Look for Plasmodium parasites.
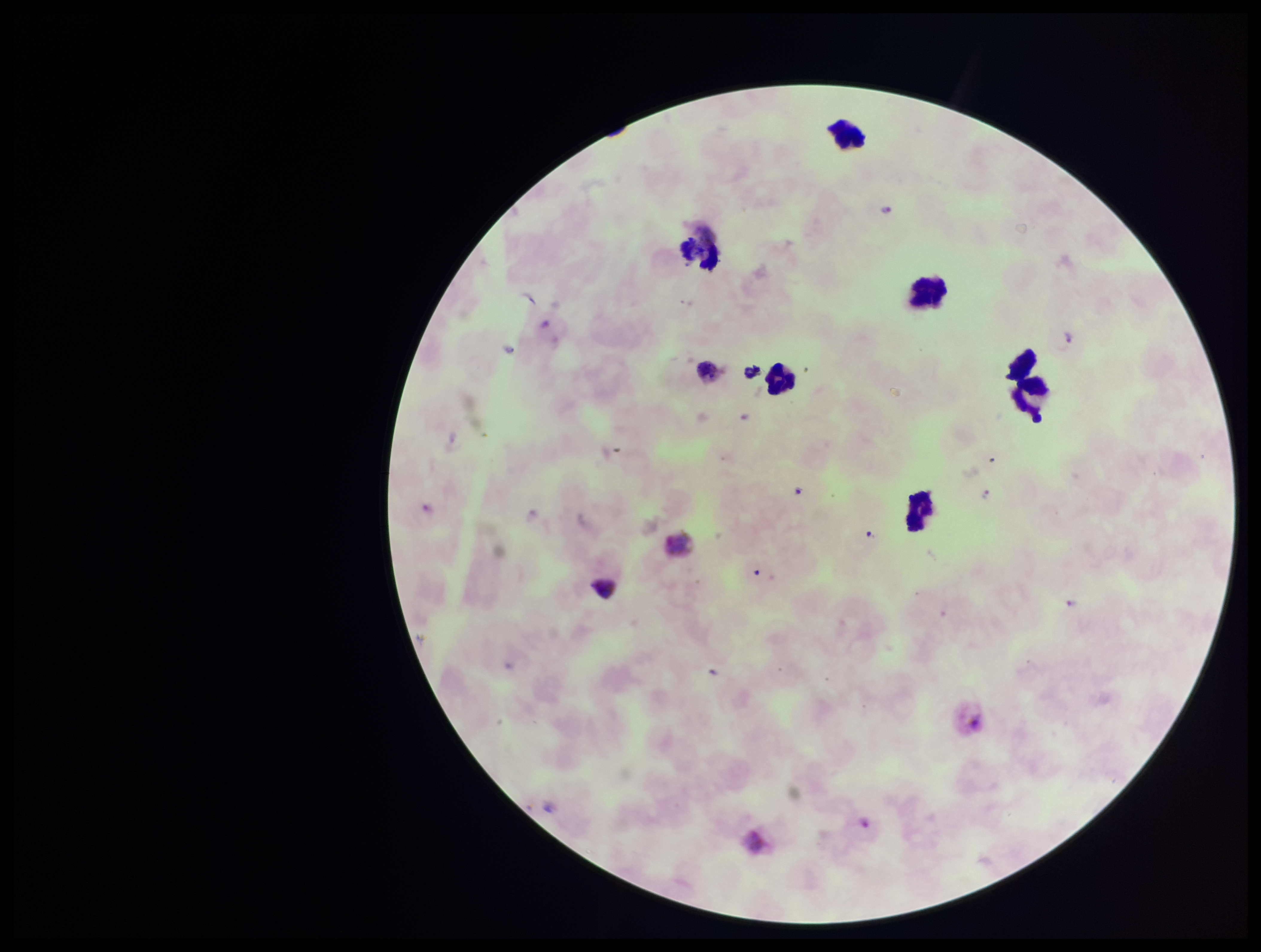

Identified.

Parasite count: 3. Patient malaria status: positive. One field from this slide. Photographed through the microscope eyepiece with a smartphone camera. Preparation: thick blood smear. Giemsa stain. Image is 1261×952 pixels. Species reported for this patient: Plasmodium vivax. Leukocyte count: 6.